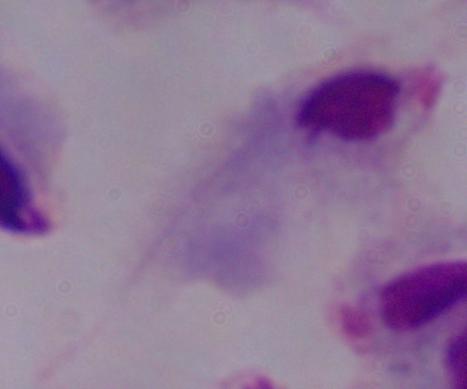

A trichomonad is shown. 1000x magnification. Micrograph.